Point out each malaria parasite.
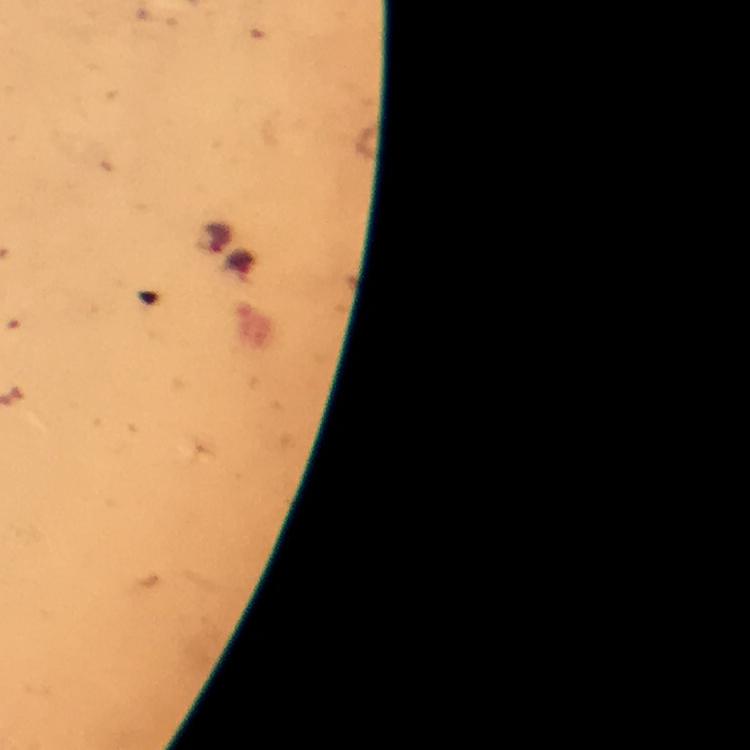

Approximate centers as {x, y} in pixels.
Malaria parasites: {215, 238}.

Giemsa-stained preparation. Thick blood film. A crop from one field of view. From a malaria diagnostic workup. Smartphone photograph taken through a microscope. Immersion oil applied. Image is 750×750 pixels. 100x magnification.